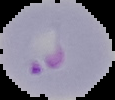

Summary:
  - Malaria status: parasitized
  - Image type: cell region segmented out of the field of view; surrounding area masked to black
  - Image size: 115×100 pixels
  - Preparation: thin blood smear